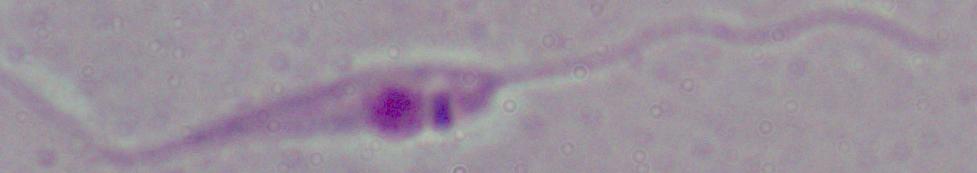

Summary:
  - Identification: Leishmania
  - Magnification: 1000x
  - Modality: photomicrograph